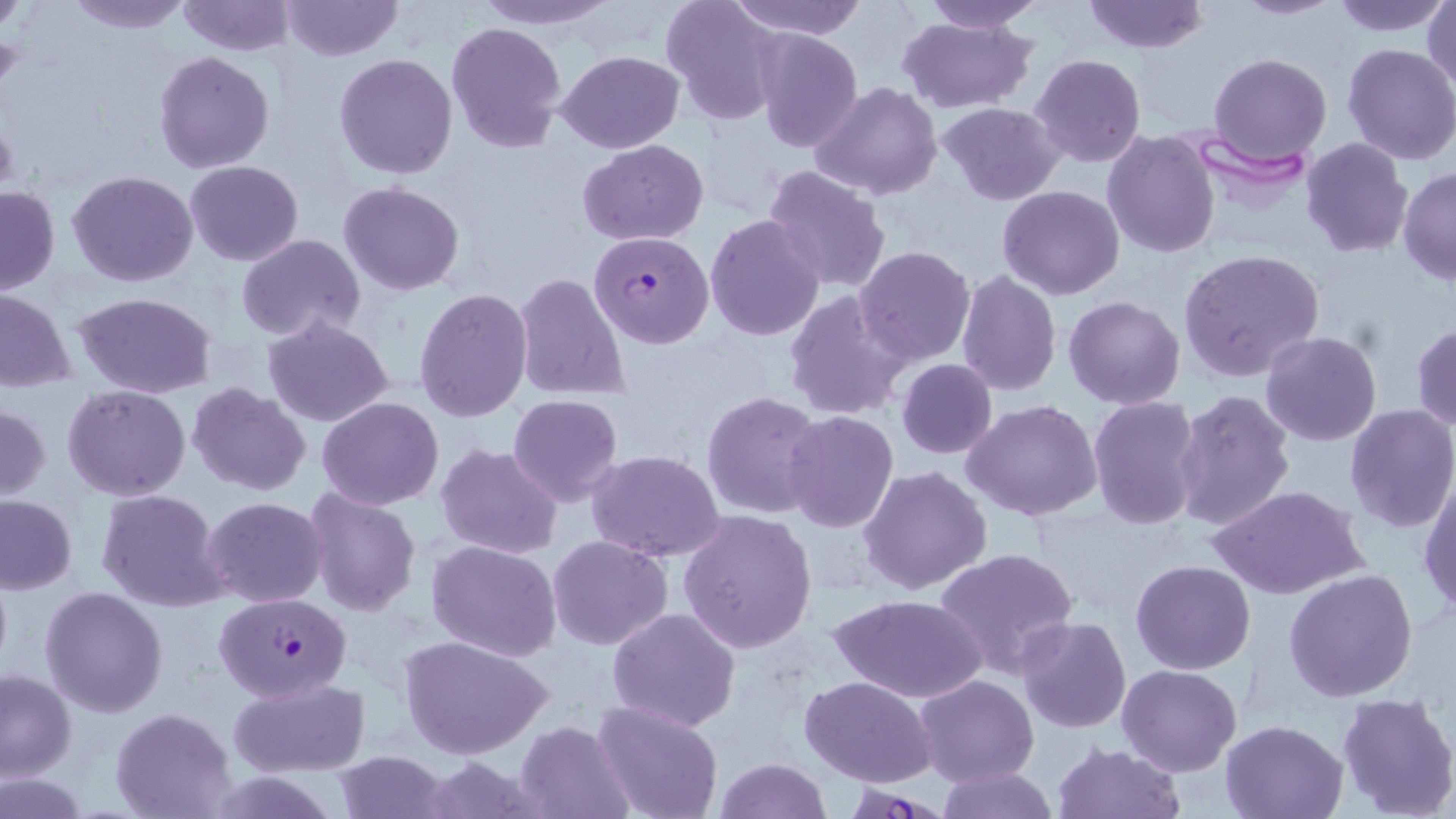

Approximate bounding boxes as named x1/y1/x2/y2 corners in pixels. Uninfected red blood cell locations: (x1=67, y1=0, x2=192, y2=34), (x1=175, y1=0, x2=297, y2=55), (x1=280, y1=0, x2=401, y2=63), (x1=472, y1=0, x2=616, y2=28), (x1=660, y1=0, x2=782, y2=125), (x1=727, y1=0, x2=869, y2=39), (x1=1081, y1=0, x2=1209, y2=53), (x1=1230, y1=0, x2=1342, y2=19), (x1=1328, y1=0, x2=1454, y2=36), (x1=1425, y1=0, x2=1456, y2=93), (x1=918, y1=1, x2=1044, y2=33), (x1=0, y1=3, x2=26, y2=33), (x1=897, y1=14, x2=1038, y2=114), (x1=446, y1=20, x2=565, y2=155), (x1=752, y1=30, x2=863, y2=151), (x1=1341, y1=43, x2=1456, y2=165), (x1=152, y1=50, x2=274, y2=174), (x1=557, y1=50, x2=683, y2=153), (x1=334, y1=53, x2=458, y2=179), (x1=1207, y1=53, x2=1332, y2=166), (x1=1030, y1=54, x2=1145, y2=168), (x1=812, y1=82, x2=942, y2=201), (x1=936, y1=101, x2=1065, y2=205), (x1=1101, y1=130, x2=1221, y2=260), (x1=1301, y1=137, x2=1413, y2=258), (x1=579, y1=139, x2=710, y2=245), (x1=186, y1=161, x2=304, y2=266), (x1=763, y1=165, x2=892, y2=293), (x1=1397, y1=166, x2=1456, y2=286), (x1=67, y1=170, x2=198, y2=288), (x1=338, y1=182, x2=466, y2=297), (x1=0, y1=184, x2=59, y2=295), (x1=997, y1=185, x2=1125, y2=299), (x1=704, y1=213, x2=826, y2=341), (x1=237, y1=234, x2=364, y2=342), (x1=855, y1=245, x2=977, y2=367), (x1=1177, y1=248, x2=1326, y2=382), (x1=514, y1=271, x2=632, y2=403), (x1=956, y1=271, x2=1062, y2=396), (x1=412, y1=287, x2=534, y2=423), (x1=0, y1=290, x2=74, y2=390), (x1=74, y1=290, x2=219, y2=397), (x1=784, y1=291, x2=913, y2=424), (x1=1063, y1=295, x2=1185, y2=408), (x1=262, y1=315, x2=393, y2=430), (x1=1411, y1=323, x2=1456, y2=431), (x1=1260, y1=331, x2=1382, y2=446), (x1=896, y1=359, x2=998, y2=458), (x1=187, y1=381, x2=312, y2=497), (x1=62, y1=386, x2=190, y2=501), (x1=1171, y1=388, x2=1296, y2=531), (x1=702, y1=389, x2=826, y2=521), (x1=507, y1=394, x2=623, y2=505), (x1=317, y1=396, x2=442, y2=509), (x1=1087, y1=396, x2=1204, y2=529), (x1=962, y1=398, x2=1103, y2=522), (x1=0, y1=404, x2=50, y2=501), (x1=1343, y1=405, x2=1456, y2=534), (x1=783, y1=411, x2=899, y2=534), (x1=436, y1=444, x2=563, y2=561), (x1=587, y1=450, x2=726, y2=562), (x1=858, y1=464, x2=993, y2=596), (x1=1418, y1=476, x2=1456, y2=617), (x1=303, y1=485, x2=421, y2=617), (x1=1212, y1=485, x2=1365, y2=600), (x1=95, y1=489, x2=228, y2=611), (x1=0, y1=493, x2=78, y2=594), (x1=201, y1=497, x2=328, y2=606), (x1=679, y1=509, x2=819, y2=653), (x1=548, y1=535, x2=674, y2=651), (x1=427, y1=541, x2=564, y2=662), (x1=933, y1=546, x2=1078, y2=678), (x1=1131, y1=559, x2=1255, y2=674), (x1=1284, y1=568, x2=1418, y2=704), (x1=40, y1=586, x2=168, y2=719), (x1=829, y1=593, x2=988, y2=704), (x1=606, y1=606, x2=741, y2=732), (x1=1016, y1=616, x2=1132, y2=734), (x1=397, y1=634, x2=555, y2=758), (x1=1117, y1=663, x2=1243, y2=775), (x1=0, y1=666, x2=77, y2=780), (x1=914, y1=675, x2=1038, y2=787), (x1=799, y1=676, x2=936, y2=787), (x1=227, y1=678, x2=370, y2=778), (x1=1335, y1=691, x2=1456, y2=819), (x1=592, y1=700, x2=724, y2=819), (x1=111, y1=708, x2=237, y2=818), (x1=1219, y1=718, x2=1350, y2=818), (x1=515, y1=720, x2=635, y2=818), (x1=1052, y1=743, x2=1185, y2=819), (x1=332, y1=751, x2=450, y2=818), (x1=713, y1=757, x2=833, y2=818), (x1=936, y1=765, x2=1060, y2=819), (x1=1, y1=773, x2=89, y2=817). Plasmodium falciparum-infected red blood cell locations: (x1=588, y1=231, x2=714, y2=349), (x1=214, y1=593, x2=352, y2=703). Slide-level diagnosis: Plasmodium falciparum. Captured at 1000x magnification. Image is 1456×819 pixels. Single field of view. Thin blood smear. Optical microscopy. May-Grünwald-Giemsa-stained preparation.